Name the cell type shown.
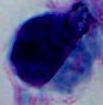

This is a leukocyte.

magnification = 1000x
modality = micrograph